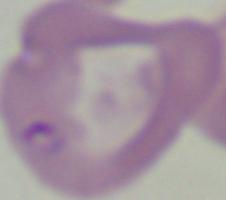

Summary:
  - Identification: Babesia
  - Magnification: 1000x
  - Modality: photomicrograph